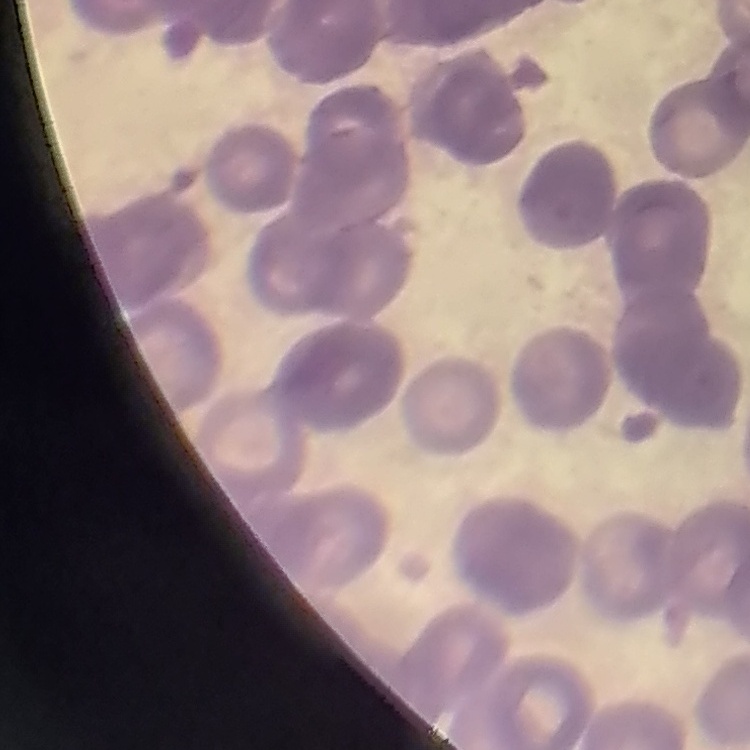 The erythrocytes show rouleaux formation. Stained with either Field's or Giemsa. Square crop of a larger photomicrograph. Thin peripheral smear.